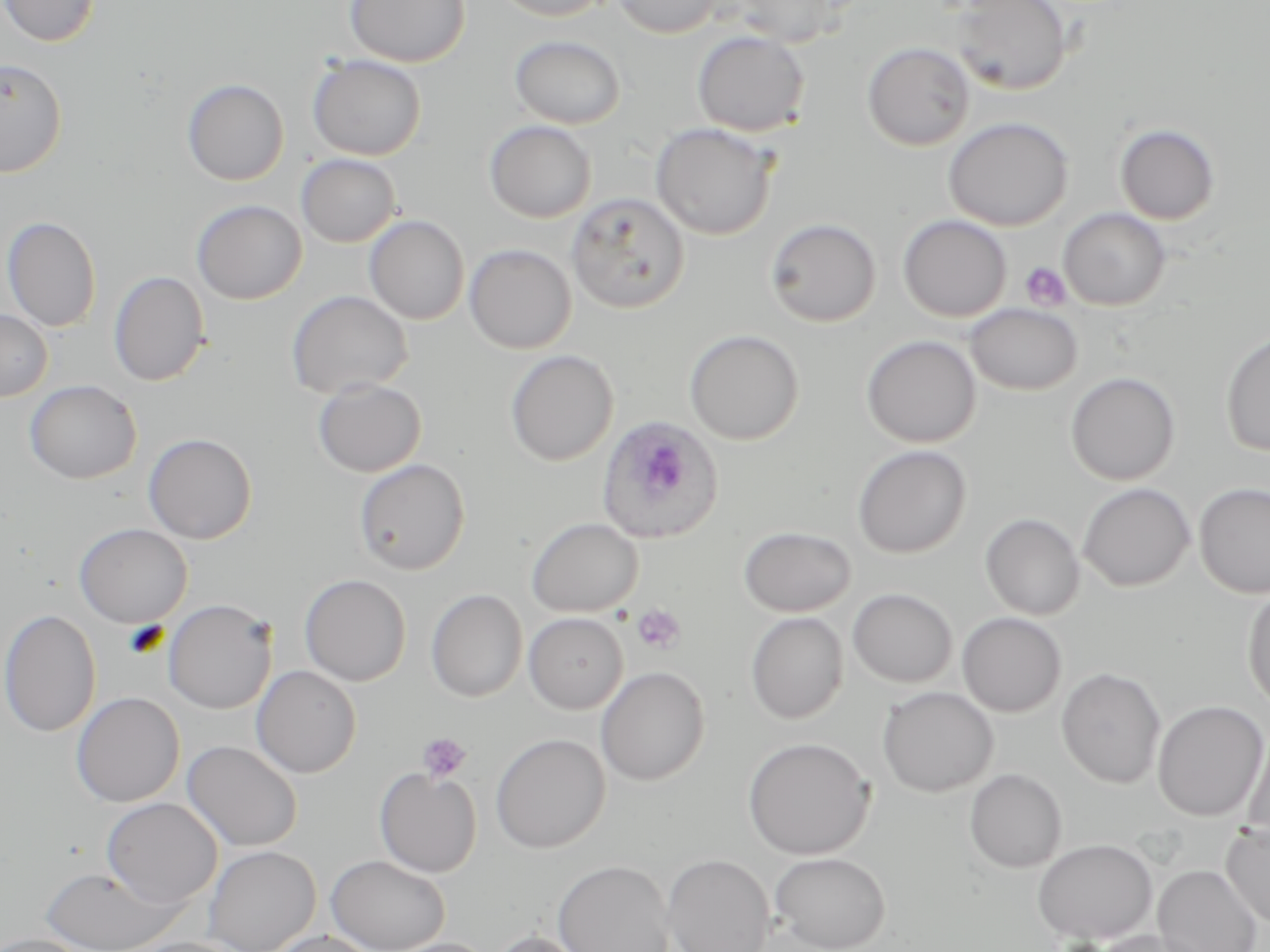 Approximate bounding boxes as (x1,y1)-(x2,y2) corner pairs in pixels. Uninfected red blood cell locations: (1,0)-(101,46), (345,0)-(470,67), (491,0)-(614,21), (612,0)-(723,38), (732,0)-(847,47), (950,0)-(1072,95), (692,30)-(810,136), (509,35)-(626,129), (862,42)-(976,151), (307,54)-(426,160), (0,58)-(68,178), (182,78)-(289,185), (943,116)-(1074,231), (484,120)-(597,223), (650,123)-(778,240), (1114,124)-(1221,225), (296,154)-(401,247), (567,193)-(691,313), (191,199)-(307,305), (1058,208)-(1170,310), (364,214)-(469,324), (1,215)-(102,332), (898,215)-(1011,321), (765,217)-(882,327), (464,243)-(577,354), (108,271)-(210,387), (286,290)-(413,399), (965,303)-(1083,395), (0,309)-(52,401), (684,329)-(804,445), (1219,331)-(1270,457), (862,335)-(981,448), (506,350)-(618,466), (1065,371)-(1181,486), (313,378)-(427,477), (24,380)-(141,483), (143,432)-(257,544), (852,444)-(972,559), (353,458)-(471,575), (1077,482)-(1195,591), (1194,482)-(1270,598), (980,512)-(1085,620), (526,517)-(644,618), (74,522)-(193,628), (739,526)-(857,617), (300,574)-(411,687), (1243,587)-(1270,712), (848,588)-(957,688), (426,589)-(528,702), (162,599)-(277,714), (0,608)-(102,738), (523,612)-(628,714), (746,612)-(849,724), (957,612)-(1066,717), (251,665)-(362,778), (595,666)-(710,786), (1056,667)-(1167,788), (877,686)-(998,797), (71,692)-(185,807), (1152,700)-(1268,821), (1242,728)-(1270,844), (491,733)-(611,853), (742,737)-(875,860), (182,740)-(303,851), (374,768)-(482,877), (964,768)-(1067,873), (101,797)-(222,908), (1220,821)-(1270,928), (1032,838)-(1158,945), (203,845)-(321,952), (770,851)-(890,952), (661,853)-(775,952), (326,854)-(451,952), (552,859)-(675,952), (1153,864)-(1262,952), (39,866)-(184,952), (1091,929)-(1209,952), (267,930)-(380,952), (486,930)-(595,952), (0,934)-(95,952), (119,938)-(246,952), (383,938)-(498,952). Plasmodium ovale-infected red blood cell locations: (598,414)-(726,544). Platelet locations: (1021,261)-(1071,311), (631,604)-(687,655), (417,732)-(472,783). Slide-level diagnosis: Plasmodium ovale. May-Grünwald-Giemsa-stained preparation. Captured at 1000x magnification. Single field of view. Optical microscopy. Thin blood film. Image is 1270×952 pixels.